Locate every leukocyte (white blood cell).
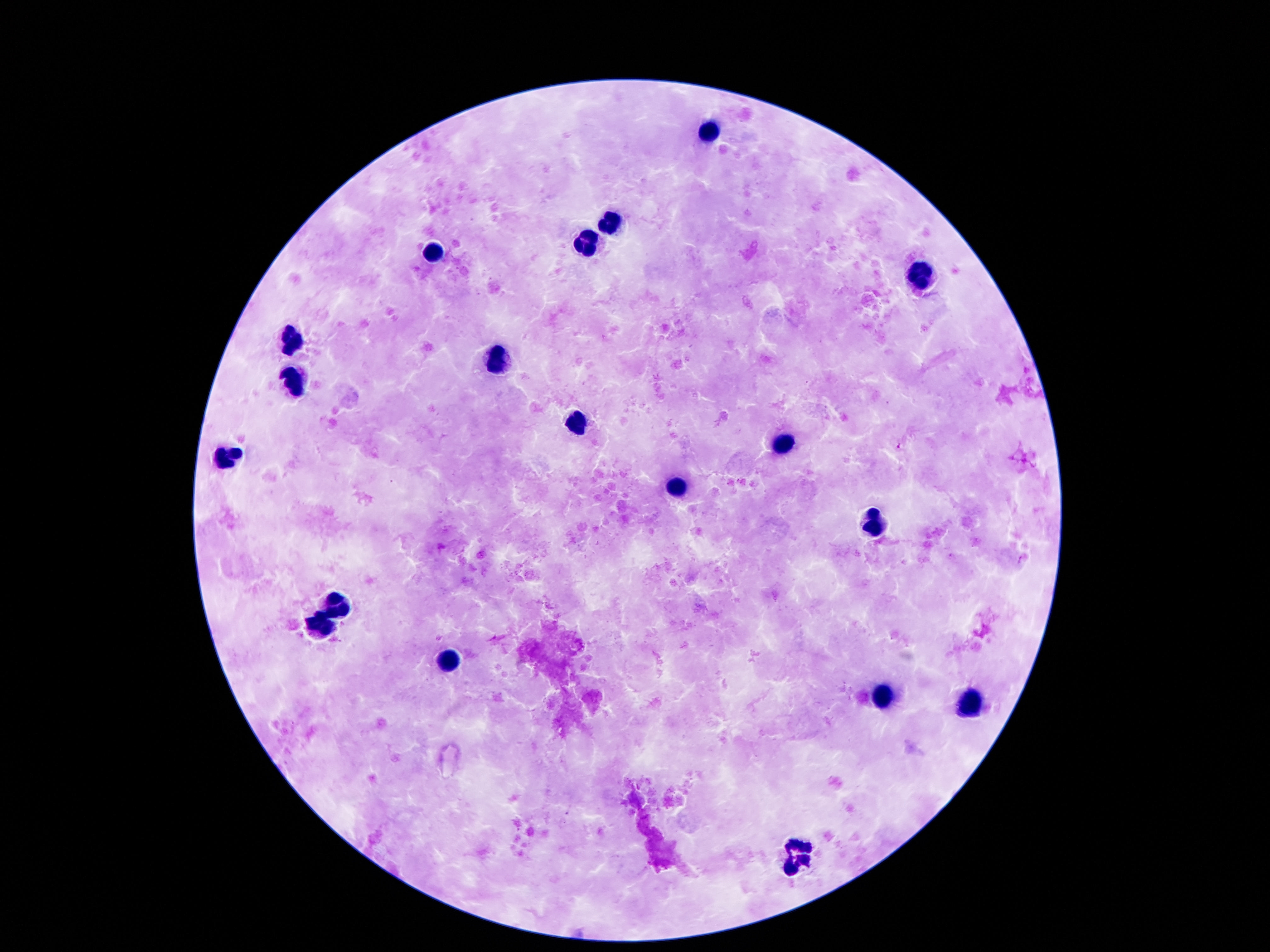

Approximate centers as {x, y} in pixels.
Leukocytes: {706, 129}, {611, 218}, {587, 245}, {436, 252}, {918, 280}, {292, 337}, {500, 358}, {297, 379}, {575, 424}, {783, 445}, {224, 459}, {677, 490}, {876, 520}, {337, 605}, {321, 624}, {447, 664}, {881, 695}, {967, 706}, {801, 854}.

{
  "patient_malaria_status": "negative",
  "magnification": "100x",
  "capture": "smartphone camera through the microscope eyepiece",
  "preparation": "thick blood film",
  "image_size": "1270×952 pixels",
  "field_of_view": "single",
  "stain": "Giemsa"
}